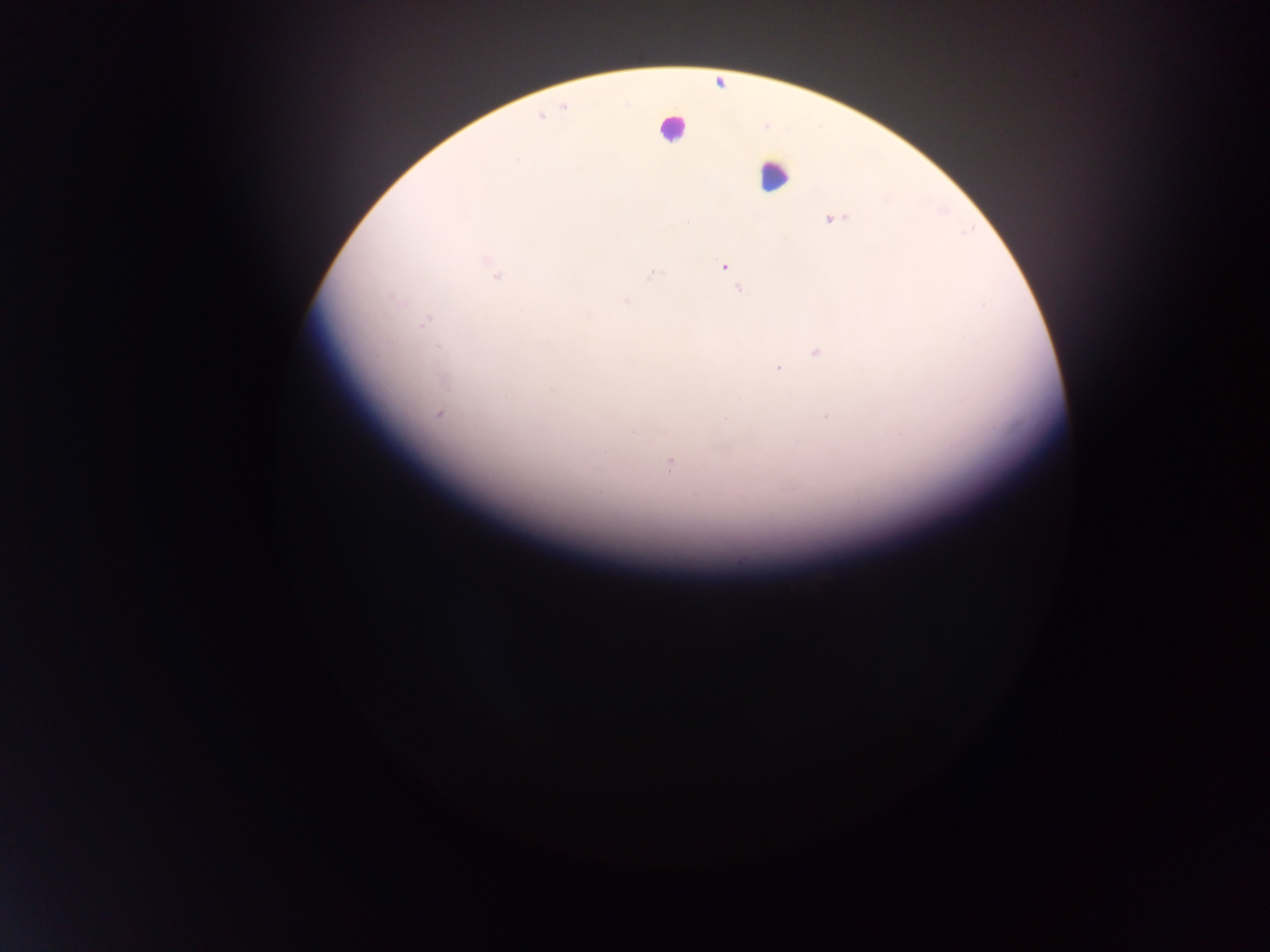 Approximate centers as {x, y} in pixels. Leukocyte locations: {672, 127}, {773, 175}. Plasmodium parasite locations: {542, 116}, {518, 159}, {833, 218}, {488, 261}, {724, 267}, {651, 273}, {496, 275}, {740, 290}, {626, 301}, {425, 323}, {438, 345}, {817, 352}, {778, 368}, {553, 390}, {439, 414}, {826, 417}, {726, 419}, {632, 433}, {670, 465}. One field of view. Sample from Ghana. Image is 1270×952 pixels. Mobile-phone photograph taken through the microscope. Thick blood smear.